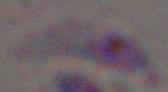
1000x magnification. Photomicrograph. Toxoplasma gondii is seen.